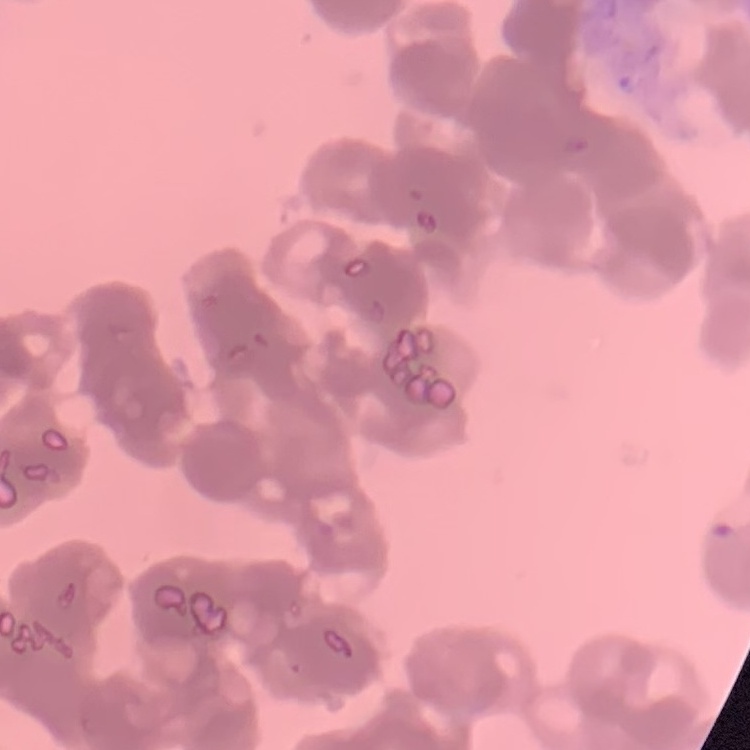

red blood cell morphology = rouleaux formation
image type = one tile cut from a larger photomicrograph
preparation = thin blood film
stain = Field's or Giemsa